Identify the blood parasite species.
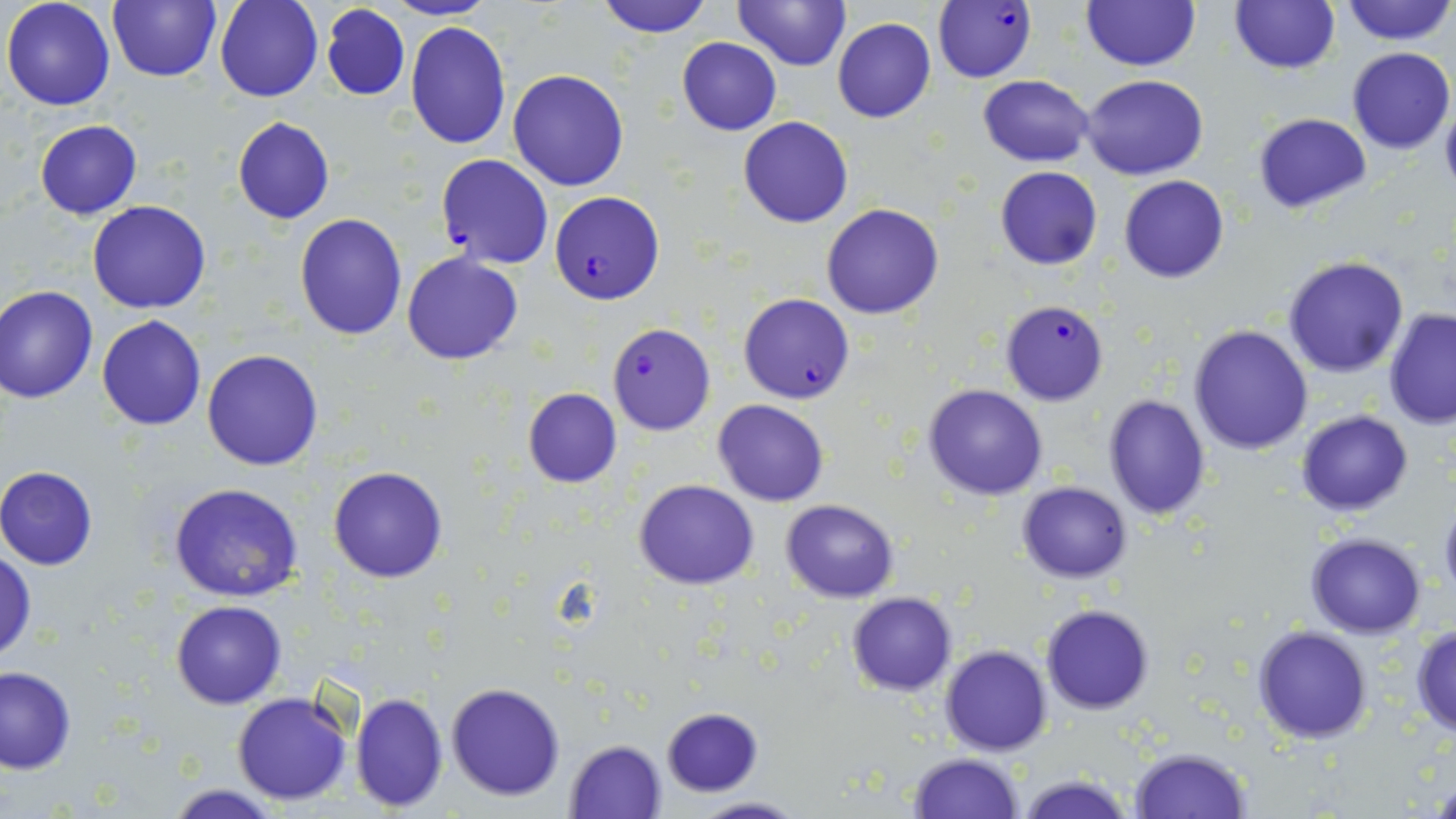

Plasmodium falciparum.

Summary:
  - Coordinate format: approximate bounding boxes as (x1,y1)-(x2,y2) corner pairs in pixels
  - Plasmodium falciparum-infected red blood cell locations: (933,0)-(1037,83), (435,153)-(553,270), (549,191)-(664,305), (738,292)-(855,403), (998,299)-(1109,406), (606,322)-(716,435)
  - Uninfected red blood cell locations: (2,0)-(117,110), (107,0)-(221,83), (214,0)-(323,101), (386,0)-(495,21), (734,0)-(850,70), (1340,0)-(1454,46), (596,1)-(712,37), (1079,1)-(1201,72), (1228,1)-(1341,75), (320,4)-(410,101), (833,16)-(937,123), (405,21)-(511,149), (677,37)-(782,135), (1348,46)-(1455,154), (507,69)-(631,191), (978,74)-(1094,165), (1081,74)-(1207,180), (1252,113)-(1371,214), (738,116)-(853,228), (232,117)-(336,225), (34,119)-(143,219), (993,166)-(1103,270), (1120,175)-(1229,283), (87,201)-(212,314), (821,203)-(945,319), (294,212)-(408,340), (401,252)-(523,365), (1282,255)-(1408,377), (0,285)-(98,402), (0,299)-(188,416), (1383,308)-(1456,428), (96,314)-(207,429), (1188,324)-(1313,454), (202,349)-(324,471), (923,385)-(1049,500), (520,388)-(624,488), (1102,394)-(1211,521), (713,398)-(829,507), (1296,409)-(1412,516), (328,466)-(448,583), (0,467)-(99,570), (634,480)-(759,588), (1015,481)-(1134,583), (169,484)-(303,602), (1438,498)-(1456,604), (781,499)-(900,601), (1305,533)-(1429,638), (0,550)-(36,663), (846,592)-(957,696), (171,599)-(286,709), (1041,604)-(1155,714), (1410,623)-(1456,740), (1252,626)-(1372,744), (939,645)-(1052,755), (0,666)-(75,774), (445,682)-(566,801), (232,692)-(353,805), (350,692)-(449,812), (661,707)-(764,796), (565,740)-(667,818), (1129,746)-(1251,818), (907,752)-(1025,819), (1017,774)-(1136,819), (1429,777)-(1455,817), (168,785)-(282,819), (686,795)-(807,818)
  - Magnification: 1000x
  - Stain: May-Grünwald-Giemsa
  - Modality: optical microscopy
  - Preparation: thin blood film
  - Image size: 1456×819 pixels
  - Field of view: one of a larger specimen